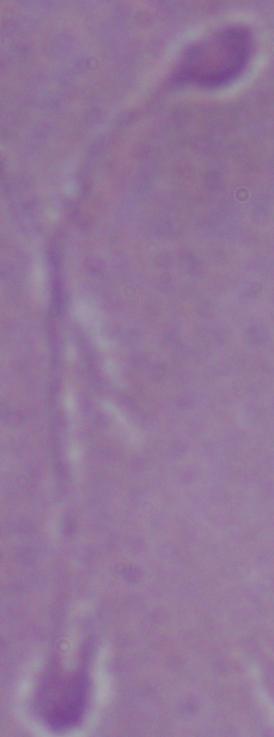
Photomicrograph. Captured at 1000x magnification. A Leishmania parasite is shown.